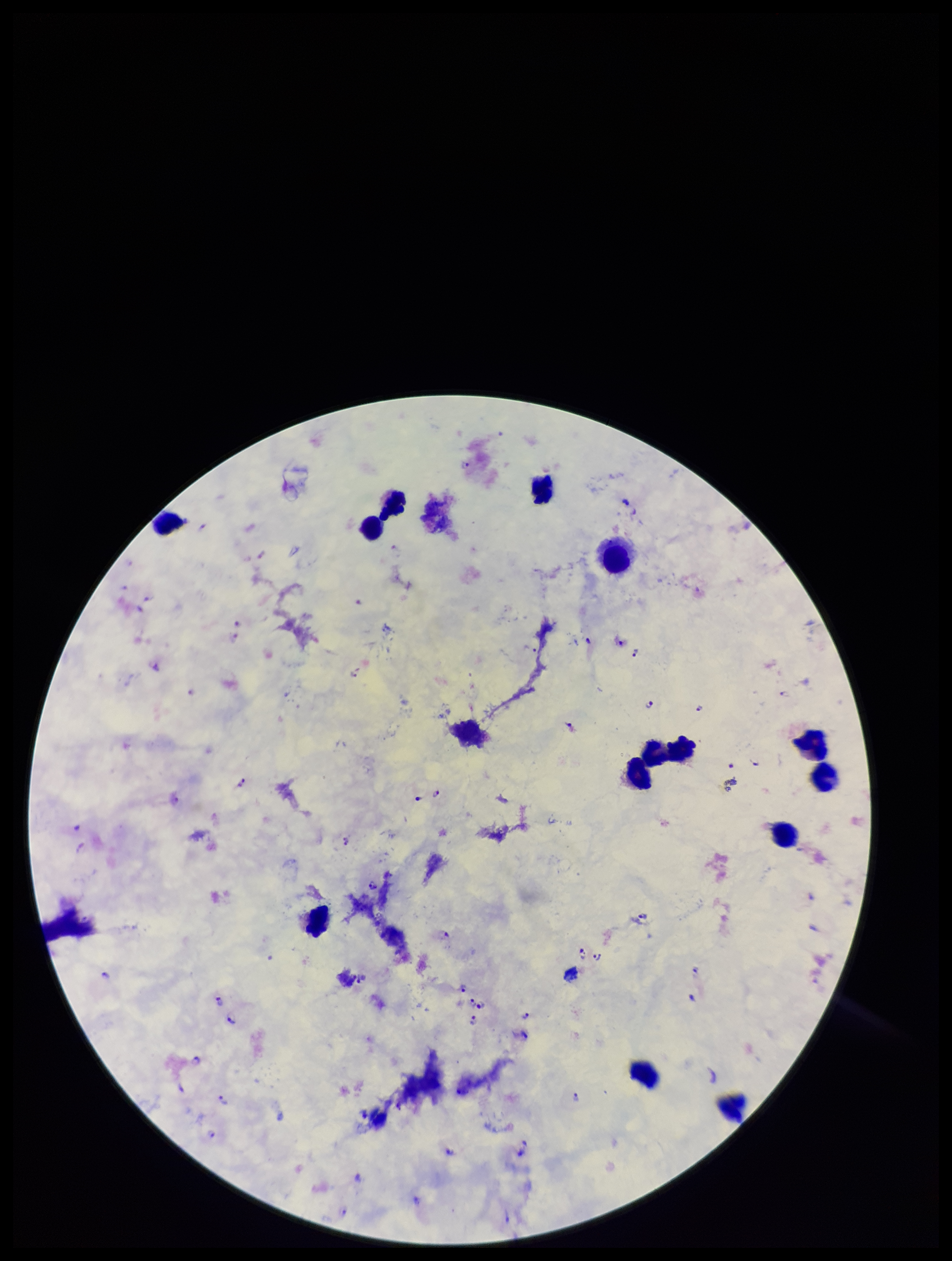
Giemsa stain. Leukocyte count: 14. Patient malaria status: positive. Species reported for this patient: Plasmodium falciparum. Single field of view. Parasite count: 35. Plasmodium parasites: detected. Photographed through the microscope eyepiece with a smartphone camera. Image is 952×1261 pixels. Preparation: thick.